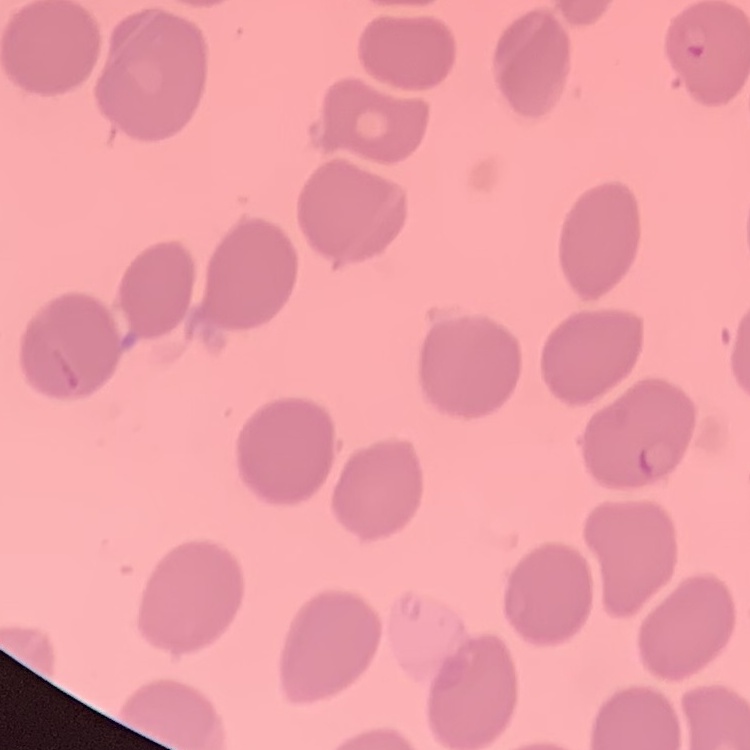
Summary:
  - Erythrocyte morphology: no rouleaux formation
  - Preparation: thin peripheral smear
  - Stain: Field's or Giemsa
  - Image type: one tile cut from a larger photomicrograph